Name the blood parasite species.
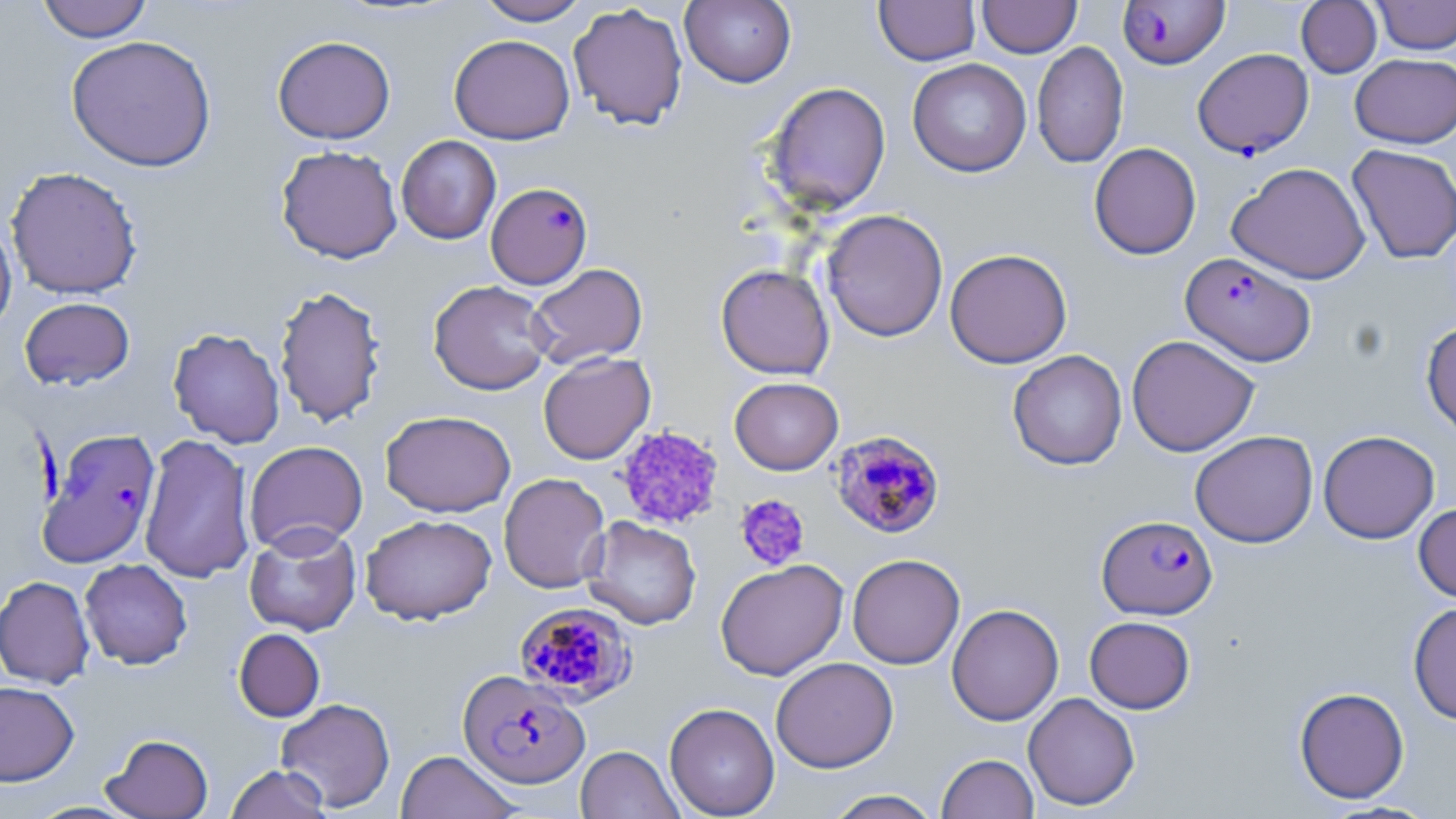

Plasmodium falciparum.

Summary:
  - Coordinate format: approximate bounding boxes as named x1/y1/x2/y2 corners in pixels
  - Uninfected red blood cell locations: (x1=36, y1=0, x2=153, y2=43), (x1=474, y1=0, x2=592, y2=25), (x1=874, y1=0, x2=980, y2=65), (x1=978, y1=0, x2=1081, y2=57), (x1=1371, y1=0, x2=1456, y2=54), (x1=680, y1=1, x2=797, y2=88), (x1=1296, y1=1, x2=1382, y2=78), (x1=568, y1=2, x2=689, y2=130), (x1=449, y1=34, x2=575, y2=144), (x1=65, y1=35, x2=217, y2=172), (x1=272, y1=35, x2=395, y2=144), (x1=1031, y1=40, x2=1129, y2=168), (x1=1350, y1=53, x2=1456, y2=148), (x1=907, y1=58, x2=1032, y2=177), (x1=765, y1=81, x2=891, y2=214), (x1=396, y1=135, x2=501, y2=244), (x1=1088, y1=142, x2=1201, y2=260), (x1=1347, y1=144, x2=1456, y2=264), (x1=276, y1=145, x2=402, y2=264), (x1=1228, y1=162, x2=1370, y2=285), (x1=5, y1=166, x2=143, y2=299), (x1=821, y1=209, x2=948, y2=342), (x1=0, y1=215, x2=17, y2=336), (x1=944, y1=248, x2=1073, y2=368), (x1=527, y1=263, x2=648, y2=369), (x1=716, y1=263, x2=834, y2=380), (x1=428, y1=280, x2=554, y2=395), (x1=274, y1=284, x2=388, y2=428), (x1=19, y1=297, x2=135, y2=390), (x1=1421, y1=320, x2=1456, y2=438), (x1=168, y1=327, x2=285, y2=448), (x1=1126, y1=334, x2=1260, y2=457), (x1=1007, y1=349, x2=1127, y2=470), (x1=538, y1=352, x2=655, y2=464), (x1=729, y1=377, x2=844, y2=475), (x1=380, y1=410, x2=516, y2=517), (x1=1190, y1=430, x2=1318, y2=548), (x1=1318, y1=430, x2=1440, y2=544), (x1=139, y1=433, x2=255, y2=584), (x1=244, y1=440, x2=368, y2=555), (x1=498, y1=473, x2=610, y2=593), (x1=1414, y1=503, x2=1456, y2=603), (x1=360, y1=513, x2=497, y2=625), (x1=582, y1=516, x2=702, y2=630), (x1=243, y1=523, x2=362, y2=636), (x1=848, y1=553, x2=965, y2=670), (x1=79, y1=558, x2=193, y2=669), (x1=715, y1=559, x2=848, y2=680), (x1=0, y1=575, x2=94, y2=689), (x1=1408, y1=602, x2=1456, y2=725), (x1=946, y1=603, x2=1064, y2=726), (x1=1084, y1=616, x2=1195, y2=714), (x1=234, y1=628, x2=325, y2=722), (x1=770, y1=656, x2=898, y2=772), (x1=0, y1=681, x2=79, y2=786), (x1=1294, y1=686, x2=1410, y2=803), (x1=1023, y1=692, x2=1140, y2=811), (x1=276, y1=697, x2=395, y2=812), (x1=664, y1=702, x2=780, y2=818), (x1=102, y1=733, x2=213, y2=818), (x1=576, y1=745, x2=683, y2=819), (x1=396, y1=750, x2=521, y2=819), (x1=936, y1=753, x2=1039, y2=818), (x1=225, y1=764, x2=332, y2=819), (x1=823, y1=789, x2=943, y2=819), (x1=25, y1=801, x2=140, y2=818)
  - Platelet locations: (x1=616, y1=425, x2=725, y2=529), (x1=735, y1=494, x2=810, y2=571)
  - Plasmodium falciparum-infected red blood cell locations: (x1=1117, y1=0, x2=1230, y2=70), (x1=1192, y1=48, x2=1314, y2=159), (x1=486, y1=182, x2=592, y2=289), (x1=1180, y1=252, x2=1316, y2=366), (x1=36, y1=428, x2=162, y2=568), (x1=830, y1=429, x2=945, y2=539), (x1=1096, y1=515, x2=1218, y2=619), (x1=513, y1=601, x2=636, y2=704), (x1=458, y1=670, x2=590, y2=788)
  - Magnification: 1000x
  - Field of view: one of a larger specimen
  - Stain: May-Grünwald-Giemsa
  - Preparation: thin blood film
  - Modality: light microscopy
  - Image size: 1456×819 pixels